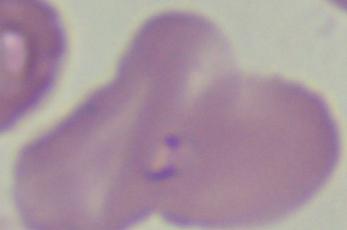

modality = photomicrograph
magnification = 1000x
identification = Babesia